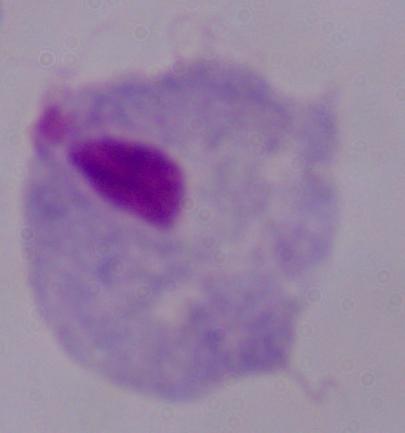
Summary:
  - Identification: trichomonad
  - Magnification: 1000x
  - Modality: micrograph